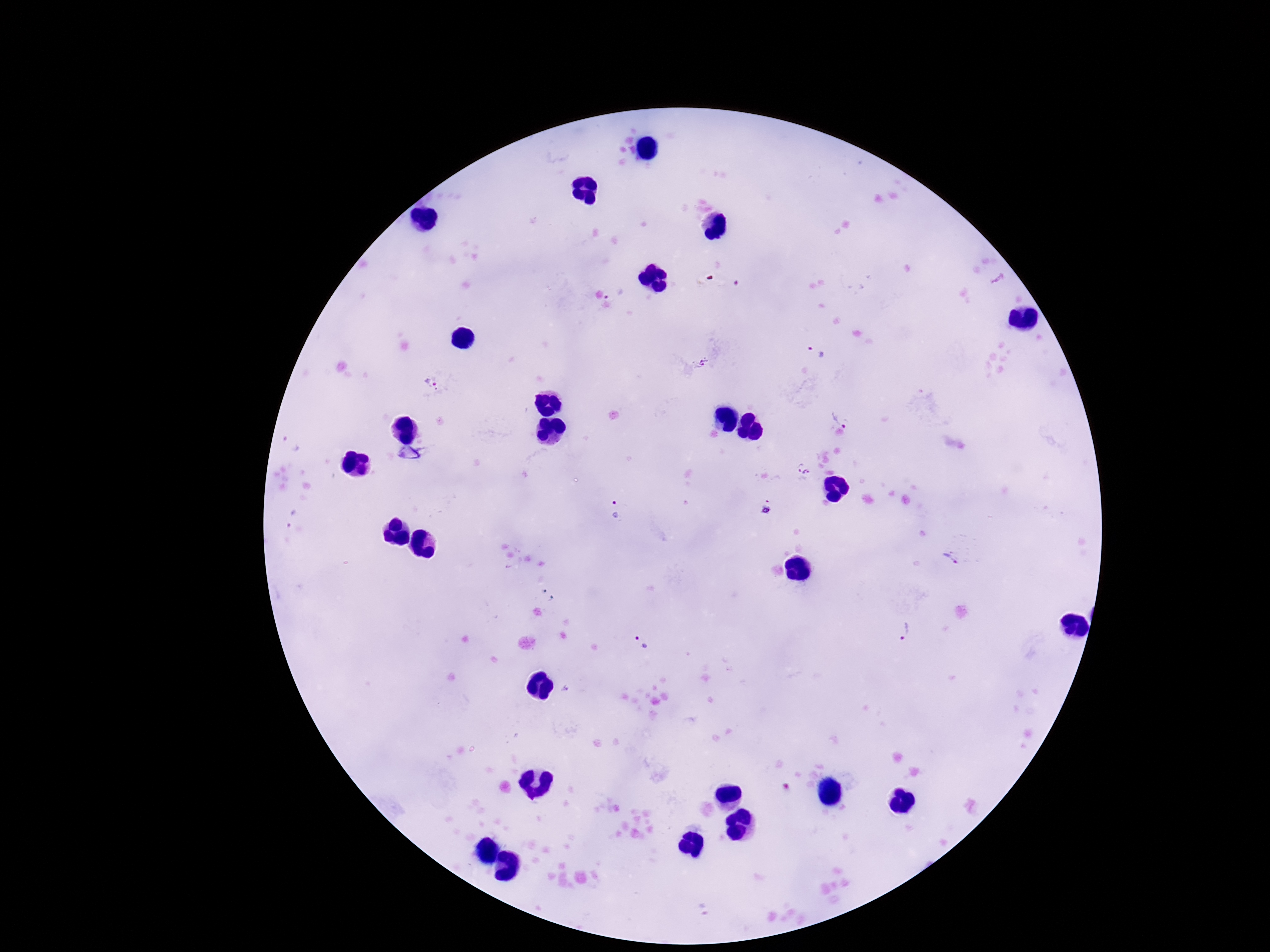

Approximate centers as {x, y} in pixels.
Summary:
  - Plasmodium parasite locations: {817, 354}, {701, 364}, {435, 385}, {844, 416}, {803, 467}, {767, 504}, {616, 511}, {952, 558}, {903, 633}, {643, 643}
  - Preparation: thick blood smear
  - Image size: 1270×952 pixels
  - Patient malaria status: infected
  - Magnification: 100x
  - Field of view: single
  - Capture: smartphone camera through the microscope eyepiece
  - Stain: Giemsa